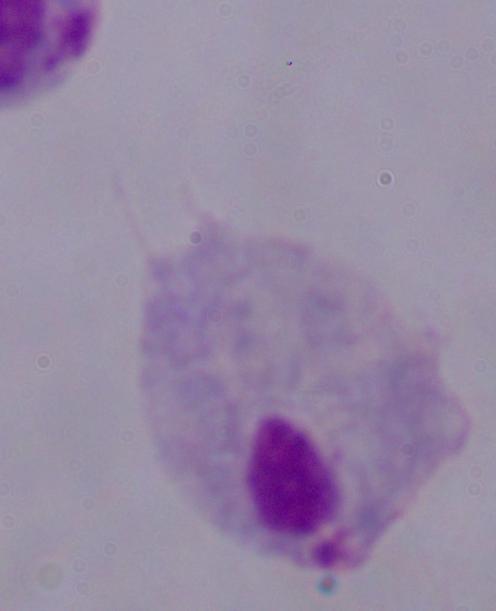
1000x magnification. A trichomonad is seen. Photomicrograph.